Locate every Plasmodium parasite.
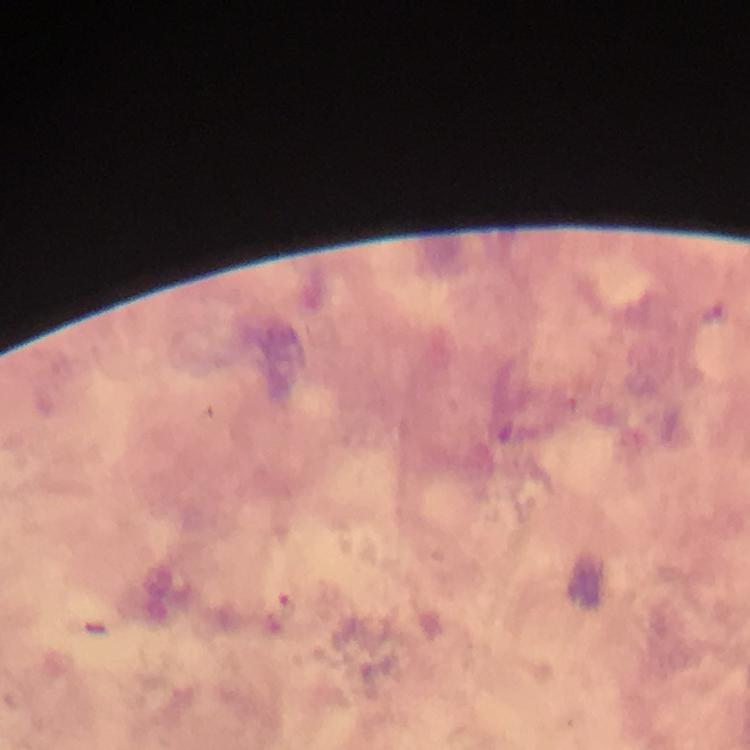
Approximate object centers, in pixels from the top-left corner.
Plasmodium parasites: (x=283, y=607).

Cropped region of a single field of view. From a malaria diagnostic workup. Photographed through the microscope with a smartphone camera. Thick blood film. Image is 750×750 pixels. Giemsa stain. At 100x magnification. Immersion oil was used.